Identify the blood parasite species.
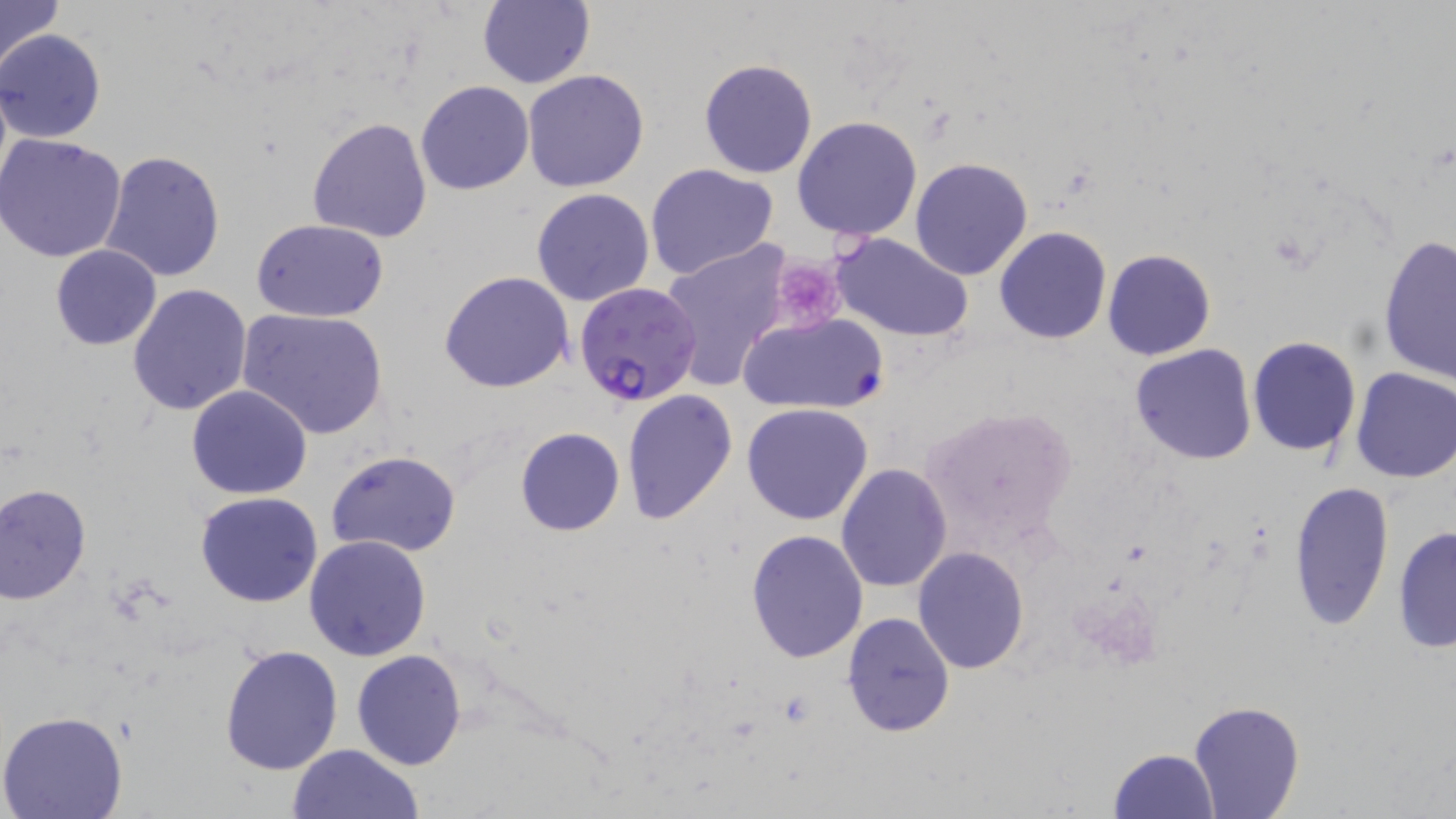

Plasmodium falciparum.

Approximate bounding boxes as named x1/y1/x2/y2 corners in pixels. Platelet locations: (x1=768, y1=257, x2=847, y2=335). Plasmodium falciparum-infected red blood cell locations: (x1=576, y1=282, x2=703, y2=406). Uninfected red blood cell locations: (x1=0, y1=0, x2=65, y2=74), (x1=478, y1=0, x2=595, y2=89), (x1=0, y1=30, x2=106, y2=144), (x1=698, y1=58, x2=818, y2=179), (x1=522, y1=69, x2=651, y2=193), (x1=415, y1=80, x2=534, y2=196), (x1=793, y1=114, x2=924, y2=242), (x1=307, y1=117, x2=433, y2=243), (x1=1, y1=134, x2=127, y2=264), (x1=99, y1=150, x2=226, y2=284), (x1=909, y1=157, x2=1034, y2=280), (x1=644, y1=163, x2=780, y2=280), (x1=530, y1=188, x2=655, y2=307), (x1=251, y1=218, x2=389, y2=323), (x1=993, y1=227, x2=1112, y2=345), (x1=828, y1=232, x2=975, y2=344), (x1=1378, y1=233, x2=1456, y2=383), (x1=660, y1=239, x2=791, y2=389), (x1=50, y1=245, x2=162, y2=350), (x1=1103, y1=249, x2=1216, y2=361), (x1=439, y1=270, x2=573, y2=393), (x1=126, y1=283, x2=253, y2=415), (x1=237, y1=307, x2=389, y2=440), (x1=739, y1=312, x2=886, y2=416), (x1=1248, y1=336, x2=1362, y2=456), (x1=1130, y1=344, x2=1257, y2=465), (x1=1350, y1=366, x2=1456, y2=484), (x1=186, y1=384, x2=312, y2=499), (x1=621, y1=389, x2=738, y2=525), (x1=742, y1=403, x2=874, y2=524), (x1=922, y1=406, x2=1080, y2=561), (x1=514, y1=428, x2=626, y2=536), (x1=325, y1=450, x2=462, y2=559), (x1=836, y1=462, x2=954, y2=592), (x1=1286, y1=479, x2=1395, y2=632), (x1=1, y1=484, x2=92, y2=604), (x1=194, y1=491, x2=325, y2=607), (x1=1391, y1=525, x2=1455, y2=653), (x1=746, y1=530, x2=869, y2=664), (x1=304, y1=534, x2=433, y2=662), (x1=911, y1=547, x2=1031, y2=674), (x1=842, y1=612, x2=955, y2=736), (x1=218, y1=642, x2=343, y2=776), (x1=351, y1=648, x2=467, y2=769), (x1=1189, y1=700, x2=1305, y2=818), (x1=0, y1=711, x2=129, y2=819), (x1=287, y1=743, x2=424, y2=819), (x1=1106, y1=749, x2=1219, y2=819). Light microscopy. May-Grünwald-Giemsa-stained preparation. One field of a larger specimen. Captured at 1000x magnification. Image is 1456×819 pixels. Thin blood film.